State which cell type is depicted.
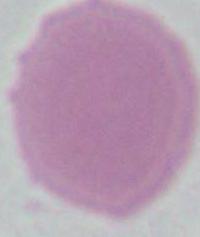

An erythrocyte.

Captured at 1000x magnification. Micrograph.